Classify this cell by malaria status.
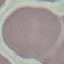
Uninfected.

capture = smartphone through the microscope eyepiece
image type = automatically extracted cell patch, resized to 64 × 64 pixels
preparation = thin blood film
stain = Giemsa